Report the malaria status of this cell.
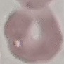

Uninfected.

capture: smartphone through the microscope eyepiece
preparation: thin blood film
image_type: cell patch, automatically extracted from a larger field of view and resized to 64 × 64 pixels
stain: Giemsa